Comment on the morphology of the red blood cells.
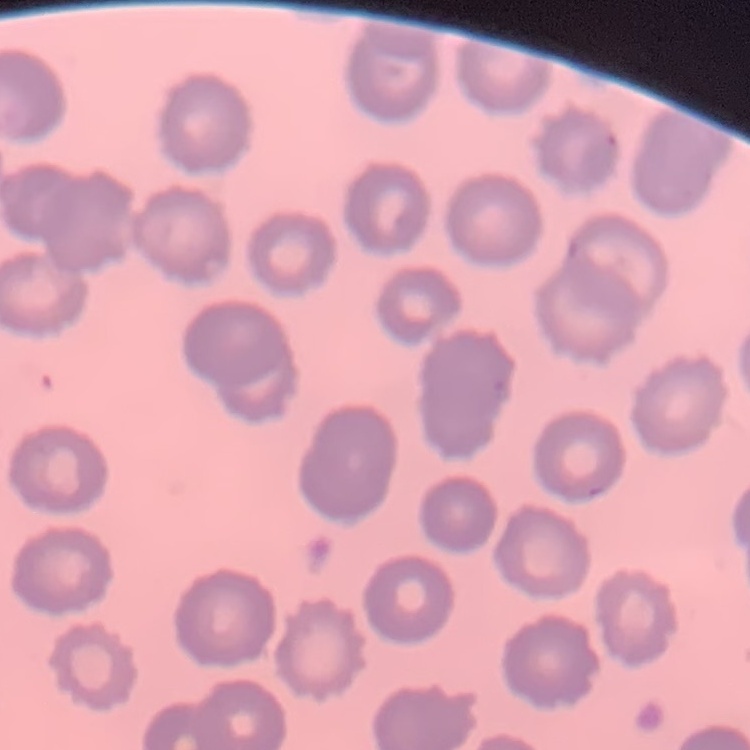
They show no rouleaux formation.

{
  "image_type": "square crop of a larger photomicrograph",
  "preparation": "thin blood film",
  "stain": "Field's or Giemsa"
}